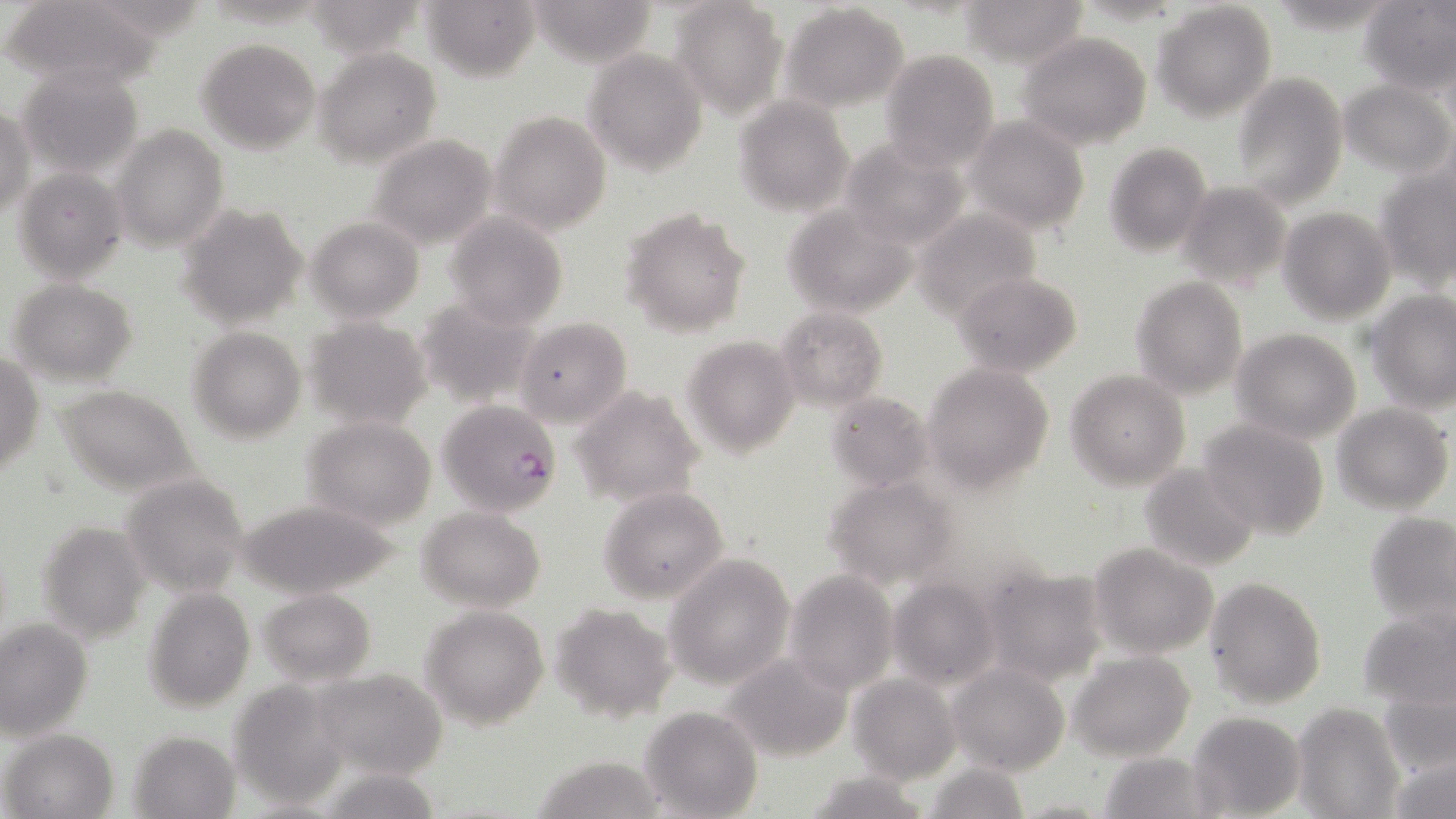
Summary:
  - Coordinate format: approximate bounding boxes as (x1,y1)-(x2,y2) corner pairs in pixels
  - Plasmodium falciparum-infected red blood cell locations: (436,399)-(562,519)
  - Uninfected red blood cell locations: (3,0)-(163,88), (423,0)-(539,81), (528,0)-(660,67), (959,0)-(1089,66), (1358,0)-(1454,94), (669,1)-(789,118), (1152,2)-(1277,122), (780,3)-(910,114), (1018,32)-(1152,149), (197,38)-(321,155), (313,48)-(442,168), (583,48)-(707,175), (880,48)-(999,170), (17,66)-(145,178), (1232,72)-(1348,207), (1341,79)-(1454,177), (733,95)-(854,216), (1,109)-(36,220), (490,110)-(611,234), (966,117)-(1090,236), (112,126)-(229,252), (366,134)-(498,249), (838,136)-(972,250), (1103,142)-(1213,256), (11,168)-(129,282), (1375,169)-(1455,290), (1175,181)-(1291,291), (781,203)-(918,318), (177,204)-(308,330), (1278,206)-(1397,325), (619,208)-(751,335), (913,209)-(1042,320), (444,213)-(568,329), (306,217)-(425,324), (951,271)-(1082,377), (1130,276)-(1248,399), (7,278)-(138,385), (1368,290)-(1456,412), (413,294)-(543,410), (774,307)-(888,412), (305,316)-(433,431), (515,319)-(632,426), (187,327)-(305,441), (1231,328)-(1362,445), (682,335)-(800,456), (0,353)-(44,475), (922,362)-(1055,491), (1064,370)-(1191,490), (54,385)-(201,496), (570,385)-(705,506), (827,391)-(934,490), (1330,402)-(1454,514), (302,416)-(438,529), (1200,420)-(1329,537), (1139,461)-(1260,573), (120,471)-(252,595), (823,476)-(960,588), (597,484)-(730,604), (234,496)-(403,600), (416,505)-(546,612), (1365,510)-(1455,625), (39,521)-(151,643), (1088,543)-(1217,659), (665,554)-(795,689), (981,567)-(1109,686), (784,569)-(899,694), (887,577)-(1001,690), (1204,577)-(1326,707), (143,585)-(255,713), (257,587)-(375,684), (549,602)-(678,722), (419,604)-(550,729), (1358,607)-(1453,707), (0,620)-(93,741), (1069,650)-(1196,762), (720,653)-(853,761), (947,663)-(1070,777), (313,668)-(448,778), (848,674)-(961,784), (226,682)-(349,808), (1381,686)-(1456,779), (1291,703)-(1405,819), (638,704)-(763,817), (1188,709)-(1306,817), (3,728)-(118,819), (129,731)-(240,816), (1386,749)-(1456,818), (1098,752)-(1211,819), (528,754)-(668,819), (924,761)-(1029,818), (804,770)-(928,819)
  - Slide-level diagnosis: Plasmodium falciparum
  - Preparation: thin blood film
  - Modality: light microscopy
  - Stain: May-Grünwald-Giemsa
  - Magnification: 1000x
  - Image size: 1456×819 pixels
  - Field of view: single